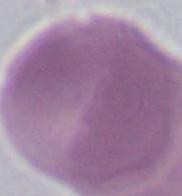

{
  "identification": "red blood cell",
  "modality": "micrograph",
  "magnification": "1000x"
}